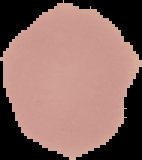

malaria status = uninfected
image size = 142×160 pixels
image type = segmented cell region on a black background
preparation = thin blood smear